Assess the morphology of the red blood cells.
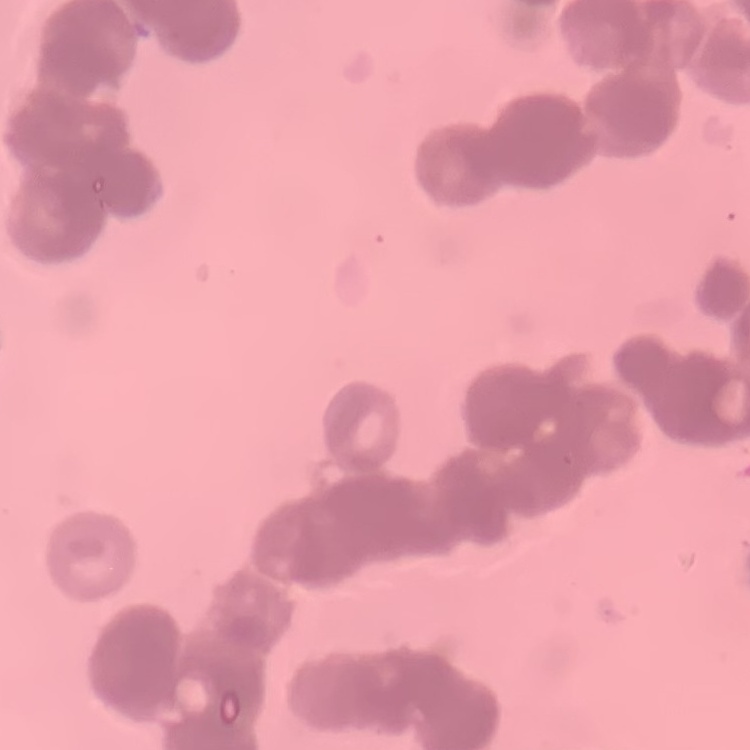
Rouleaux formation.

Thin peripheral smear. Square crop of a larger photomicrograph. Field's or Giemsa stain.